Locate every malaria parasite.
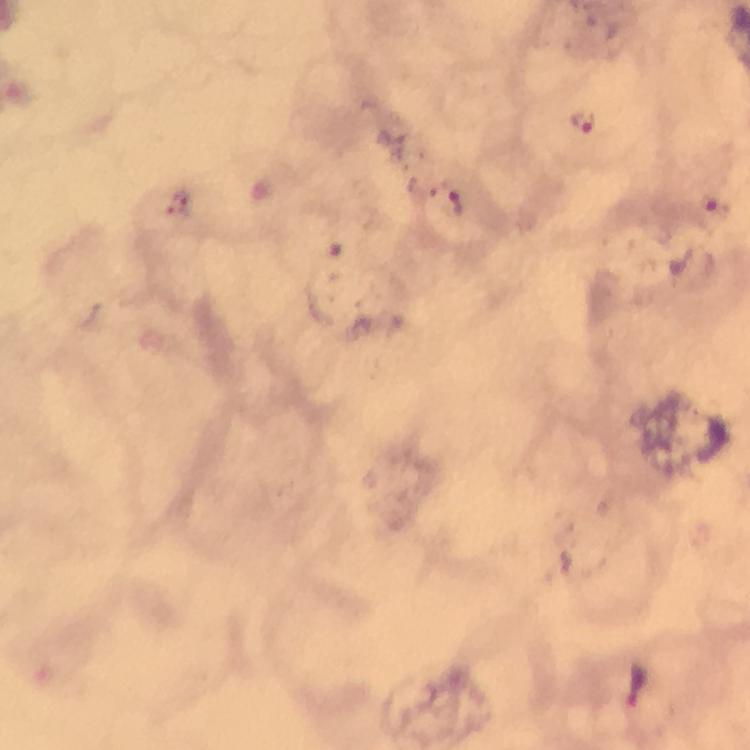
Approximate centers as [x, y] in pixels.
Malaria parasites: [580, 122], [457, 199], [634, 682].

Photographed through the microscope with a smartphone camera. Thick blood smear. Immersion oil applied. At 100x magnification. From a diagnostic examination for malaria. Image is 750×750 pixels. Giemsa-stained preparation. A crop from one field of view.